Give the extent of all Plasmodium ovale-infected red blood cells.
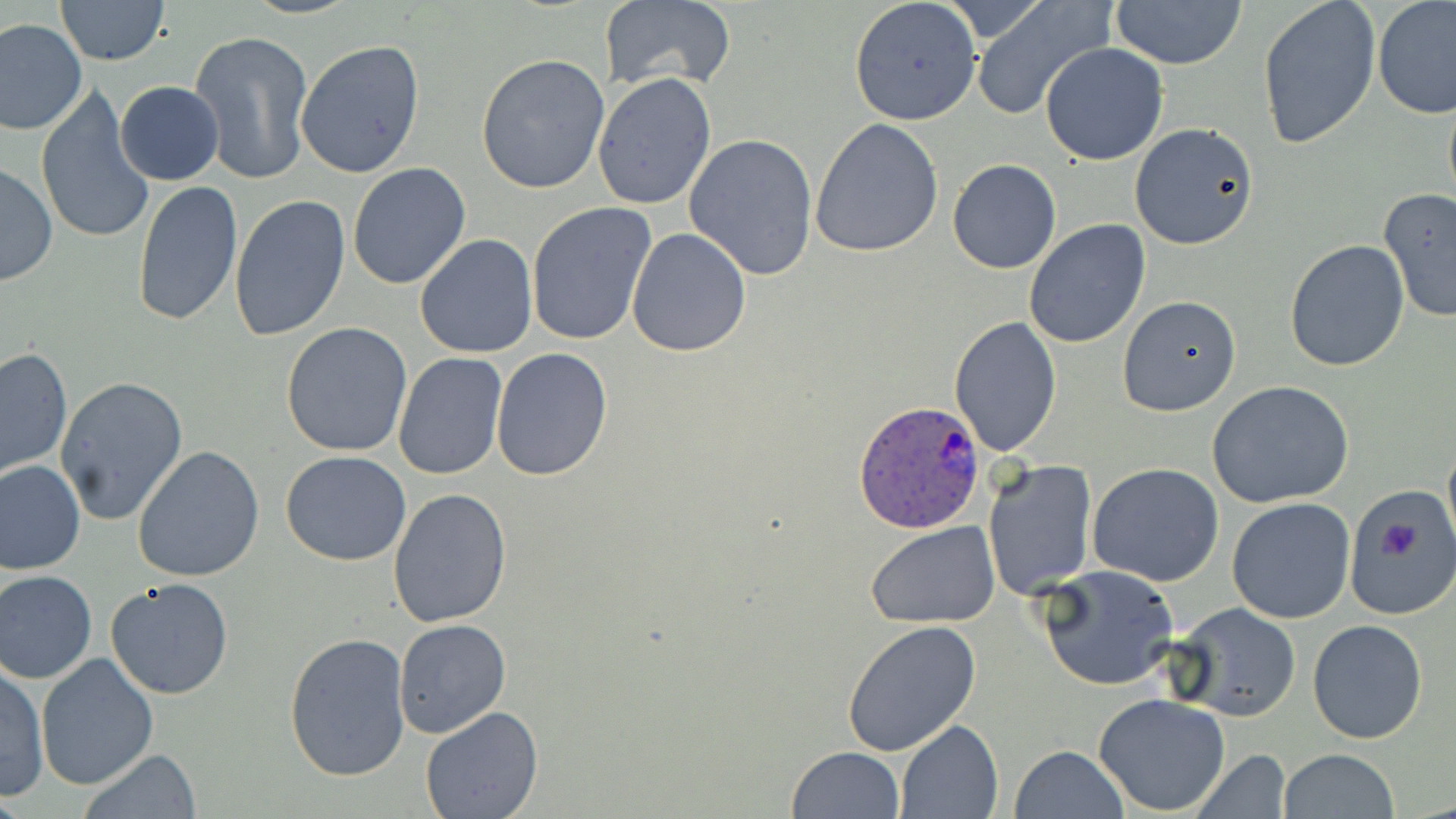

Approximate bounding boxes as named x1/y1/x2/y2 corners in pixels.
Plasmodium ovale-infected red blood cells: (x1=853, y1=400, x2=985, y2=533).

Platelet locations: (x1=1374, y1=511, x2=1423, y2=563). Uninfected red blood cell locations: (x1=54, y1=0, x2=169, y2=66), (x1=242, y1=0, x2=357, y2=19), (x1=598, y1=0, x2=736, y2=94), (x1=848, y1=0, x2=982, y2=125), (x1=1111, y1=0, x2=1248, y2=70), (x1=1257, y1=0, x2=1381, y2=150), (x1=1374, y1=0, x2=1456, y2=119), (x1=970, y1=1, x2=1114, y2=119), (x1=0, y1=18, x2=87, y2=135), (x1=188, y1=30, x2=315, y2=189), (x1=295, y1=39, x2=425, y2=180), (x1=1040, y1=43, x2=1168, y2=166), (x1=475, y1=54, x2=609, y2=195), (x1=591, y1=72, x2=717, y2=212), (x1=114, y1=82, x2=223, y2=185), (x1=1442, y1=83, x2=1456, y2=220), (x1=37, y1=87, x2=158, y2=247), (x1=810, y1=118, x2=944, y2=258), (x1=1128, y1=122, x2=1259, y2=249), (x1=684, y1=134, x2=819, y2=281), (x1=947, y1=158, x2=1061, y2=273), (x1=1, y1=161, x2=57, y2=287), (x1=348, y1=162, x2=472, y2=289), (x1=133, y1=179, x2=243, y2=327), (x1=1378, y1=188, x2=1456, y2=322), (x1=227, y1=194, x2=350, y2=345), (x1=525, y1=201, x2=657, y2=346), (x1=1024, y1=220, x2=1149, y2=350), (x1=625, y1=227, x2=751, y2=358), (x1=414, y1=234, x2=539, y2=359), (x1=1283, y1=238, x2=1410, y2=373), (x1=1117, y1=294, x2=1243, y2=417), (x1=949, y1=317, x2=1062, y2=456), (x1=281, y1=323, x2=412, y2=457), (x1=2, y1=347, x2=71, y2=480), (x1=491, y1=347, x2=613, y2=482), (x1=393, y1=352, x2=507, y2=480), (x1=55, y1=376, x2=188, y2=525), (x1=1207, y1=380, x2=1355, y2=508), (x1=133, y1=445, x2=266, y2=582), (x1=281, y1=450, x2=412, y2=566), (x1=982, y1=458, x2=1099, y2=601), (x1=0, y1=459, x2=85, y2=574), (x1=1087, y1=463, x2=1224, y2=587), (x1=1349, y1=485, x2=1454, y2=617), (x1=388, y1=489, x2=513, y2=629), (x1=1227, y1=496, x2=1357, y2=624), (x1=866, y1=523, x2=999, y2=628), (x1=1036, y1=564, x2=1180, y2=691), (x1=0, y1=570, x2=98, y2=684), (x1=107, y1=578, x2=234, y2=700), (x1=1171, y1=603, x2=1302, y2=721), (x1=392, y1=618, x2=512, y2=739), (x1=1308, y1=619, x2=1429, y2=745), (x1=842, y1=621, x2=983, y2=758), (x1=284, y1=631, x2=412, y2=781), (x1=36, y1=654, x2=159, y2=791), (x1=1, y1=661, x2=48, y2=800), (x1=1092, y1=692, x2=1231, y2=816), (x1=420, y1=705, x2=543, y2=819), (x1=896, y1=719, x2=1003, y2=819), (x1=787, y1=745, x2=905, y2=819), (x1=1009, y1=745, x2=1128, y2=819), (x1=77, y1=748, x2=202, y2=818), (x1=1188, y1=749, x2=1291, y2=818), (x1=1278, y1=749, x2=1400, y2=818). Slide-level diagnosis: Plasmodium ovale. Light microscopy. Captured at 1000x magnification. Image is 1456×819 pixels. May-Grünwald-Giemsa-stained preparation. Thin blood smear. One field of a larger specimen.